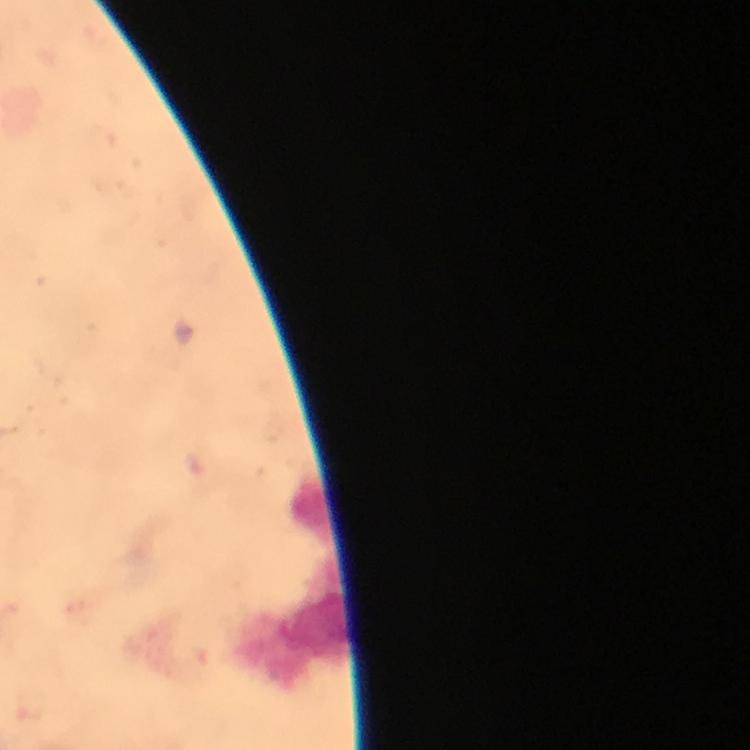
Approximate centers as {x, y} in pixels. Malaria parasite locations: {35, 703}. Leukocyte locations: {309, 510}, {314, 625}. Image is 750×750 pixels. Smartphone photograph taken through a microscope. From a diagnostic examination for malaria. At 100x magnification. Immersion oil was used. Thick blood smear. A crop from one field of view. Giemsa stain.